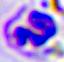
Summary:
  - Modality: micrograph
  - Identification: leukocyte
  - Magnification: 400x